State the blood parasite species.
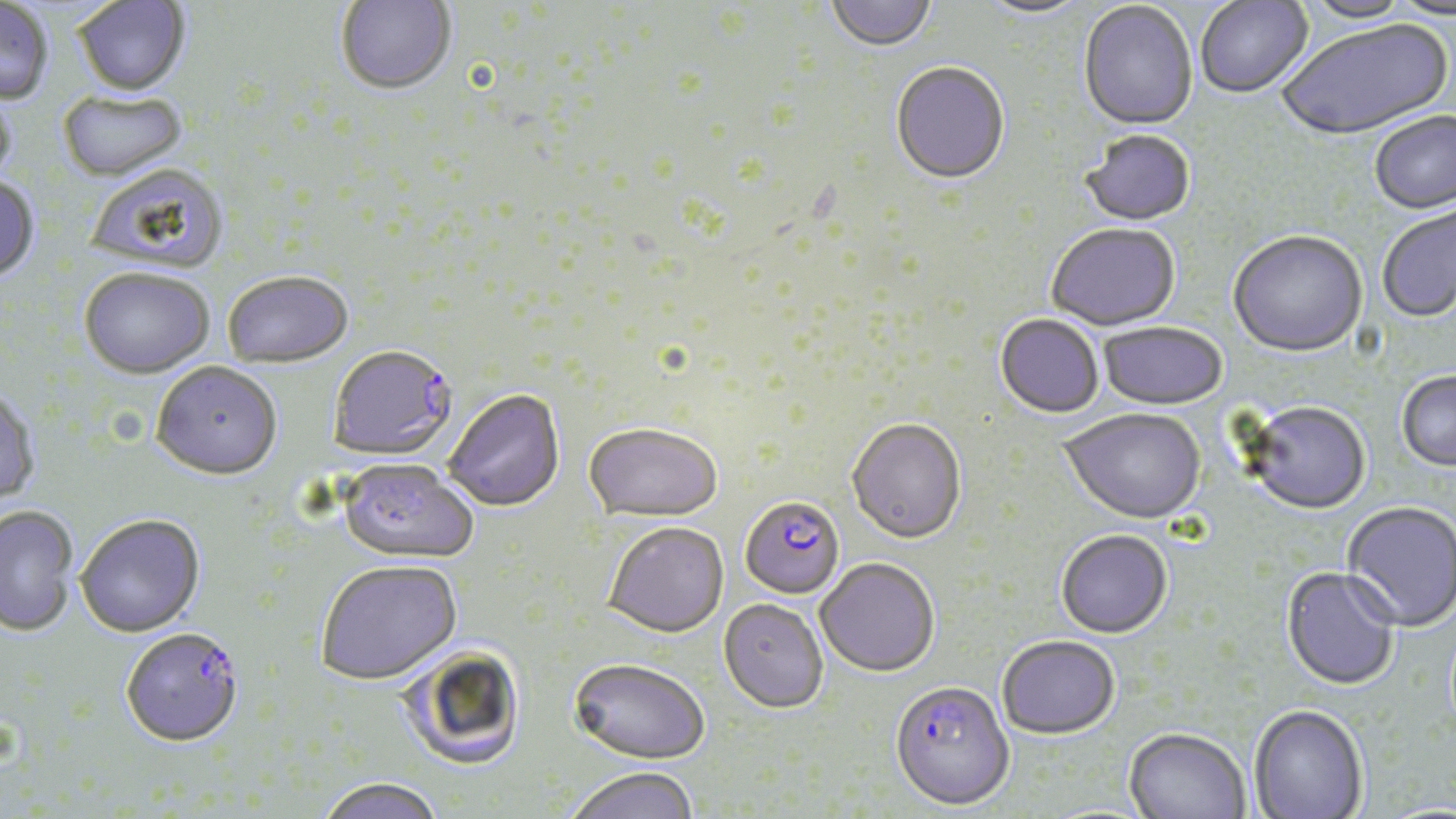

Plasmodium falciparum.

Approximate bounding boxes as named x1/y1/x2/y2 corners in pixels. Plasmodium falciparum-infected red blood cell locations: (x1=327, y1=344, x2=456, y2=459), (x1=739, y1=495, x2=845, y2=599), (x1=120, y1=629, x2=245, y2=748), (x1=889, y1=680, x2=1015, y2=810). Uninfected red blood cell locations: (x1=336, y1=0, x2=457, y2=97), (x1=825, y1=0, x2=937, y2=53), (x1=1196, y1=0, x2=1314, y2=100), (x1=1301, y1=0, x2=1416, y2=25), (x1=1387, y1=0, x2=1456, y2=22), (x1=74, y1=1, x2=191, y2=99), (x1=977, y1=1, x2=1095, y2=20), (x1=0, y1=2, x2=54, y2=106), (x1=1078, y1=2, x2=1198, y2=132), (x1=1278, y1=19, x2=1454, y2=143), (x1=890, y1=64, x2=1010, y2=188), (x1=0, y1=90, x2=17, y2=192), (x1=58, y1=91, x2=187, y2=183), (x1=1369, y1=113, x2=1456, y2=217), (x1=1080, y1=131, x2=1196, y2=228), (x1=86, y1=165, x2=230, y2=277), (x1=0, y1=177, x2=40, y2=286), (x1=1378, y1=203, x2=1455, y2=324), (x1=1046, y1=225, x2=1181, y2=333), (x1=1228, y1=232, x2=1369, y2=360), (x1=79, y1=270, x2=214, y2=381), (x1=222, y1=272, x2=354, y2=369), (x1=994, y1=315, x2=1103, y2=420), (x1=1097, y1=324, x2=1227, y2=412), (x1=150, y1=362, x2=282, y2=481), (x1=1397, y1=372, x2=1456, y2=474), (x1=0, y1=388, x2=40, y2=508), (x1=443, y1=388, x2=565, y2=512), (x1=1242, y1=403, x2=1372, y2=517), (x1=1059, y1=410, x2=1206, y2=527), (x1=846, y1=419, x2=967, y2=546), (x1=583, y1=422, x2=723, y2=521), (x1=337, y1=459, x2=479, y2=564), (x1=1341, y1=502, x2=1455, y2=633), (x1=0, y1=506, x2=78, y2=637), (x1=76, y1=514, x2=205, y2=638), (x1=602, y1=521, x2=729, y2=637), (x1=1056, y1=530, x2=1173, y2=640), (x1=816, y1=558, x2=940, y2=677), (x1=315, y1=559, x2=461, y2=686), (x1=1281, y1=568, x2=1399, y2=693), (x1=718, y1=598, x2=828, y2=713), (x1=997, y1=637, x2=1120, y2=741), (x1=399, y1=645, x2=526, y2=772), (x1=568, y1=657, x2=710, y2=764), (x1=1249, y1=706, x2=1369, y2=819), (x1=1124, y1=730, x2=1250, y2=819), (x1=562, y1=765, x2=699, y2=819), (x1=316, y1=777, x2=444, y2=819). May-Grünwald-Giemsa-stained preparation. Captured at 1000x magnification. Image is 1456×819 pixels. Optical microscopy. One field of a larger specimen. Thin blood film.